Mark where platelets are.
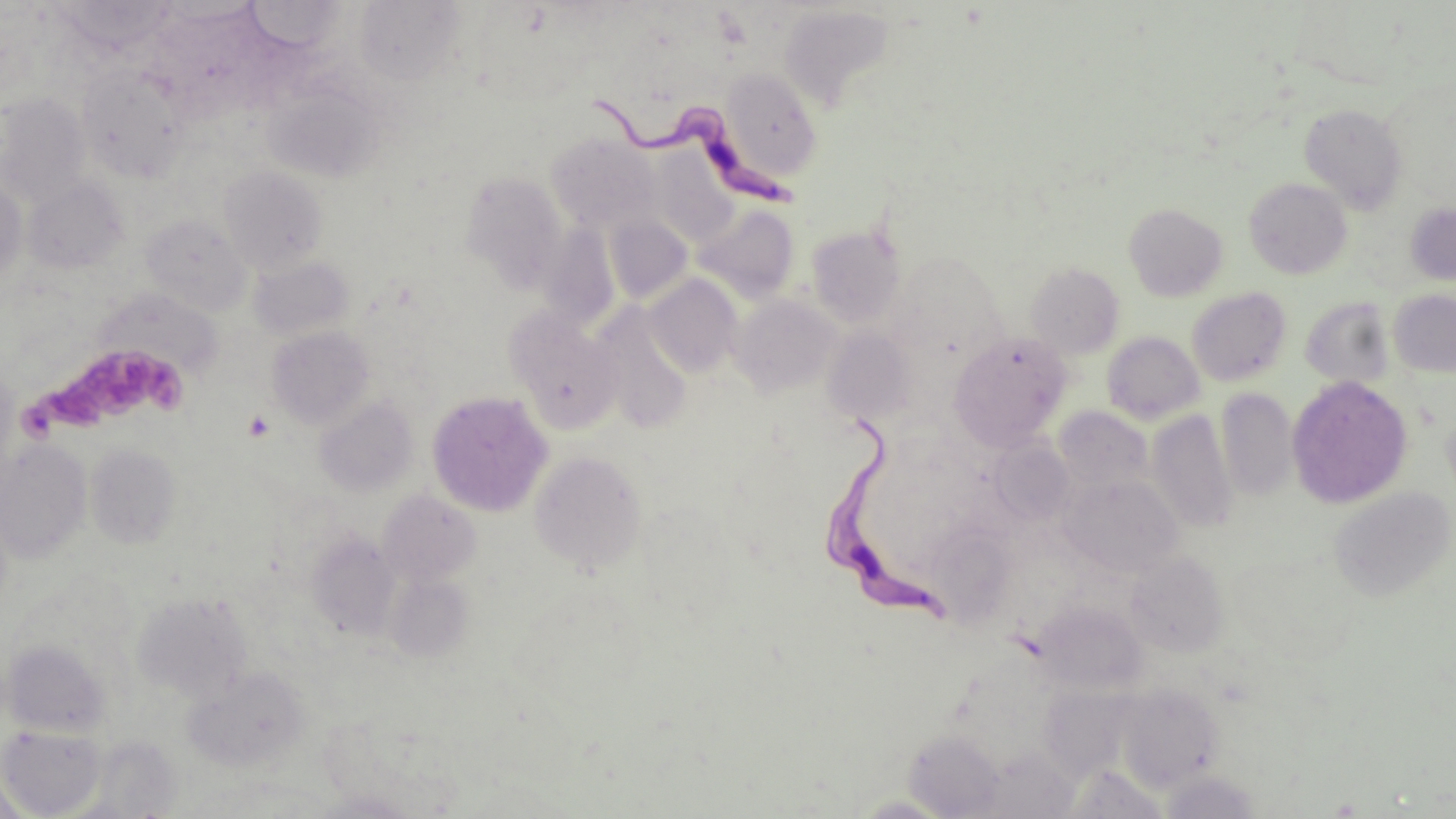

Approximate bounding boxes as named x1/y1/x2/y2 corners in pixels.
Platelets: (x1=30, y1=341, x2=188, y2=433), (x1=242, y1=410, x2=275, y2=441).

slide_level_diagnosis: Trypanosoma brucei
magnification: 1000x
trypanosoma_brucei_locations: 'approximate bounding boxes as named x1/y1/x2/y2 corners in pixels: (x1=586, y1=92, x2=796, y2=210), (x1=824, y1=407, x2=953, y2=627)'
uninfected_red_blood_cell_locations: 'approximate bounding boxes as named x1/y1/x2/y2 corners in pixels: (x1=53, y1=0, x2=179, y2=54), (x1=245, y1=1, x2=346, y2=52), (x1=354, y1=1, x2=465, y2=86), (x1=779, y1=3, x2=895, y2=111), (x1=76, y1=64, x2=189, y2=182), (x1=719, y1=68, x2=822, y2=181), (x1=263, y1=77, x2=385, y2=182), (x1=0, y1=94, x2=92, y2=207), (x1=1299, y1=103, x2=1409, y2=213), (x1=548, y1=134, x2=660, y2=234), (x1=648, y1=149, x2=738, y2=246), (x1=219, y1=166, x2=329, y2=273), (x1=461, y1=172, x2=570, y2=291), (x1=24, y1=177, x2=129, y2=274), (x1=1244, y1=177, x2=1352, y2=279), (x1=0, y1=178, x2=27, y2=286), (x1=1405, y1=202, x2=1456, y2=287), (x1=1124, y1=203, x2=1228, y2=302), (x1=695, y1=204, x2=800, y2=301), (x1=141, y1=214, x2=251, y2=316), (x1=603, y1=215, x2=693, y2=304), (x1=806, y1=223, x2=908, y2=329), (x1=537, y1=224, x2=620, y2=332), (x1=889, y1=252, x2=1005, y2=360), (x1=249, y1=254, x2=354, y2=341), (x1=1026, y1=262, x2=1124, y2=358), (x1=644, y1=277, x2=743, y2=377), (x1=1186, y1=287, x2=1292, y2=387), (x1=1388, y1=289, x2=1456, y2=378), (x1=731, y1=294, x2=842, y2=398), (x1=1300, y1=297, x2=1396, y2=390), (x1=592, y1=306, x2=693, y2=432), (x1=505, y1=308, x2=624, y2=433), (x1=266, y1=325, x2=374, y2=429), (x1=822, y1=328, x2=918, y2=424), (x1=1102, y1=331, x2=1205, y2=424), (x1=949, y1=332, x2=1072, y2=451), (x1=0, y1=363, x2=20, y2=485), (x1=1286, y1=375, x2=1413, y2=509), (x1=1216, y1=388, x2=1299, y2=502), (x1=427, y1=390, x2=553, y2=517), (x1=314, y1=396, x2=418, y2=497), (x1=1054, y1=406, x2=1152, y2=493), (x1=1147, y1=410, x2=1238, y2=533), (x1=987, y1=438, x2=1075, y2=525), (x1=0, y1=440, x2=93, y2=563), (x1=86, y1=444, x2=182, y2=549), (x1=529, y1=450, x2=647, y2=574), (x1=1062, y1=474, x2=1184, y2=579), (x1=1328, y1=486, x2=1455, y2=603), (x1=378, y1=491, x2=481, y2=585), (x1=307, y1=532, x2=403, y2=639), (x1=1125, y1=551, x2=1229, y2=657), (x1=386, y1=573, x2=474, y2=661), (x1=132, y1=592, x2=253, y2=701), (x1=1033, y1=601, x2=1147, y2=693), (x1=3, y1=640, x2=110, y2=737), (x1=183, y1=667, x2=310, y2=773), (x1=1116, y1=682, x2=1223, y2=790), (x1=1038, y1=686, x2=1132, y2=778), (x1=323, y1=715, x2=463, y2=815), (x1=1, y1=724, x2=107, y2=817), (x1=904, y1=728, x2=1006, y2=818), (x1=1160, y1=769, x2=1261, y2=818), (x1=0, y1=778, x2=31, y2=819), (x1=307, y1=790, x2=422, y2=818)'
modality: light microscopy
field_of_view: one of a larger specimen
image_size: 1456×819 pixels
stain: May-Grünwald-Giemsa
preparation: thin blood film